Locate every blood parasite and identify its species.
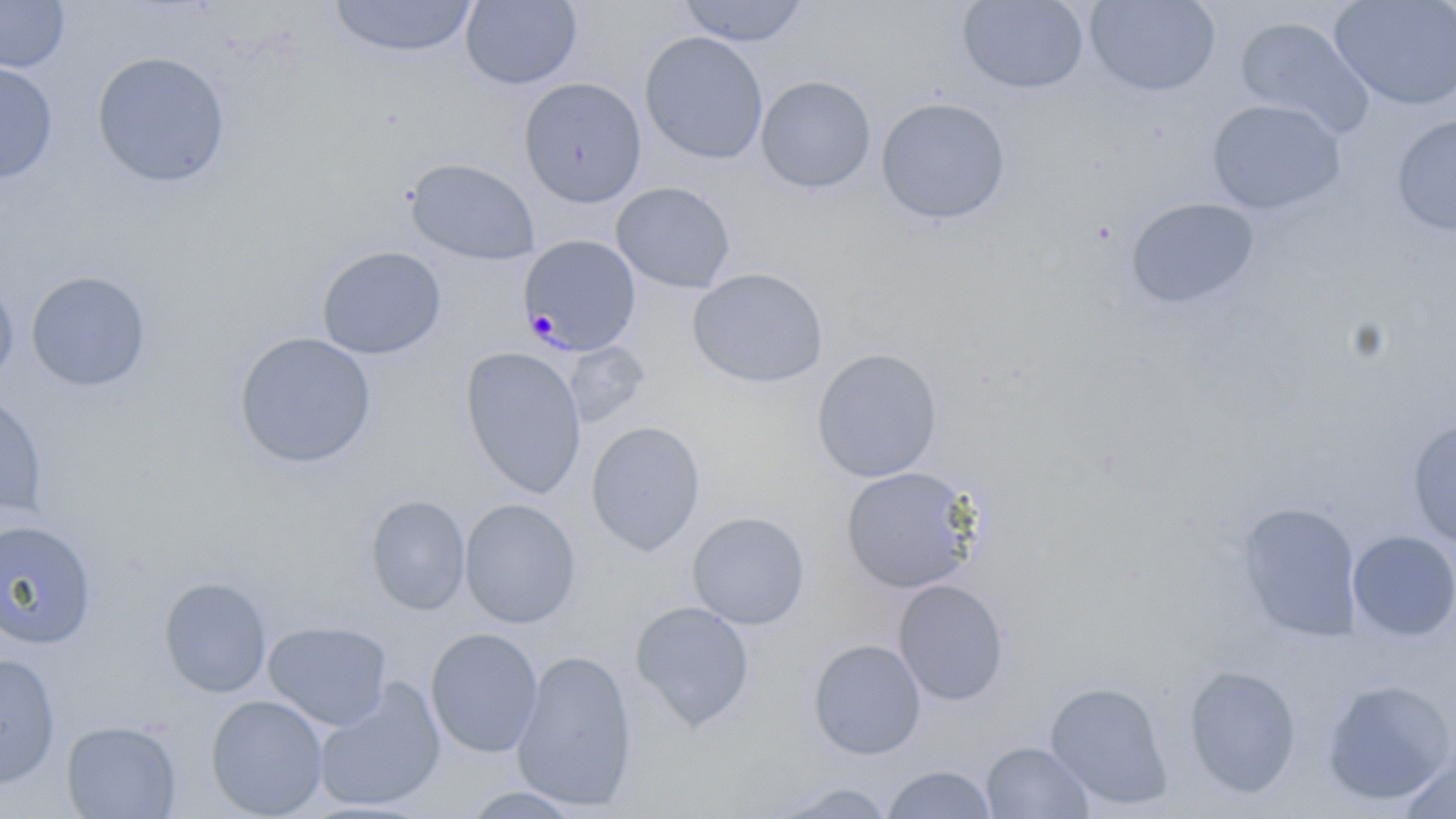
Approximate bounding boxes as named x1/y1/x2/y2 corners in pixels.
Plasmodium malariae-infected red blood cells: (x1=518, y1=235, x2=641, y2=356).
No Plasmodium falciparum, Plasmodium ovale, Plasmodium vivax, Babesia divergens, or Trypanosoma brucei observed.

Uninfected red blood cell locations: (x1=328, y1=0, x2=478, y2=60), (x1=676, y1=0, x2=811, y2=47), (x1=1084, y1=0, x2=1221, y2=96), (x1=1330, y1=0, x2=1456, y2=111), (x1=0, y1=1, x2=70, y2=74), (x1=460, y1=1, x2=582, y2=90), (x1=958, y1=1, x2=1089, y2=95), (x1=1235, y1=16, x2=1375, y2=139), (x1=640, y1=31, x2=768, y2=165), (x1=91, y1=51, x2=230, y2=187), (x1=0, y1=62, x2=58, y2=183), (x1=756, y1=75, x2=876, y2=193), (x1=518, y1=77, x2=647, y2=207), (x1=876, y1=97, x2=1011, y2=224), (x1=1206, y1=99, x2=1346, y2=215), (x1=1391, y1=114, x2=1456, y2=235), (x1=405, y1=158, x2=539, y2=265), (x1=611, y1=181, x2=735, y2=293), (x1=1126, y1=197, x2=1259, y2=309), (x1=316, y1=245, x2=447, y2=359), (x1=688, y1=268, x2=828, y2=389), (x1=25, y1=271, x2=151, y2=392), (x1=0, y1=274, x2=18, y2=387), (x1=232, y1=331, x2=377, y2=468), (x1=564, y1=342, x2=649, y2=427), (x1=460, y1=347, x2=587, y2=498), (x1=811, y1=348, x2=942, y2=483), (x1=0, y1=391, x2=48, y2=521), (x1=1406, y1=418, x2=1456, y2=550), (x1=586, y1=421, x2=705, y2=556), (x1=839, y1=466, x2=980, y2=593), (x1=366, y1=495, x2=470, y2=616), (x1=459, y1=498, x2=581, y2=629), (x1=1238, y1=502, x2=1362, y2=640), (x1=687, y1=511, x2=810, y2=630), (x1=0, y1=519, x2=98, y2=649), (x1=1347, y1=530, x2=1456, y2=641), (x1=158, y1=576, x2=272, y2=698), (x1=894, y1=579, x2=1009, y2=705), (x1=630, y1=601, x2=755, y2=730), (x1=263, y1=621, x2=392, y2=731), (x1=425, y1=627, x2=543, y2=758), (x1=808, y1=640, x2=926, y2=760), (x1=511, y1=651, x2=637, y2=811), (x1=0, y1=653, x2=60, y2=789), (x1=1183, y1=664, x2=1302, y2=798), (x1=312, y1=679, x2=446, y2=812), (x1=1044, y1=680, x2=1174, y2=809), (x1=1320, y1=680, x2=1455, y2=806), (x1=205, y1=694, x2=329, y2=818), (x1=60, y1=719, x2=182, y2=819), (x1=1396, y1=740, x2=1456, y2=819), (x1=980, y1=741, x2=1095, y2=818), (x1=881, y1=765, x2=998, y2=819), (x1=768, y1=782, x2=899, y2=818), (x1=458, y1=786, x2=590, y2=818). Slide-level diagnosis: Plasmodium malariae. Image is 1456×819 pixels. May-Grünwald-Giemsa-stained preparation. One field of a larger specimen. Thin blood film. Light microscopy. Captured at 1000x magnification.